Assess this cell for malaria.
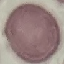

Uninfected.

Cell patch, automatically extracted from a larger field of view and resized to 64 × 64 pixels. Giemsa stain. Acquired by smartphone through the microscope eyepiece. Thin blood film.